Comment on the morphology of the erythrocytes.
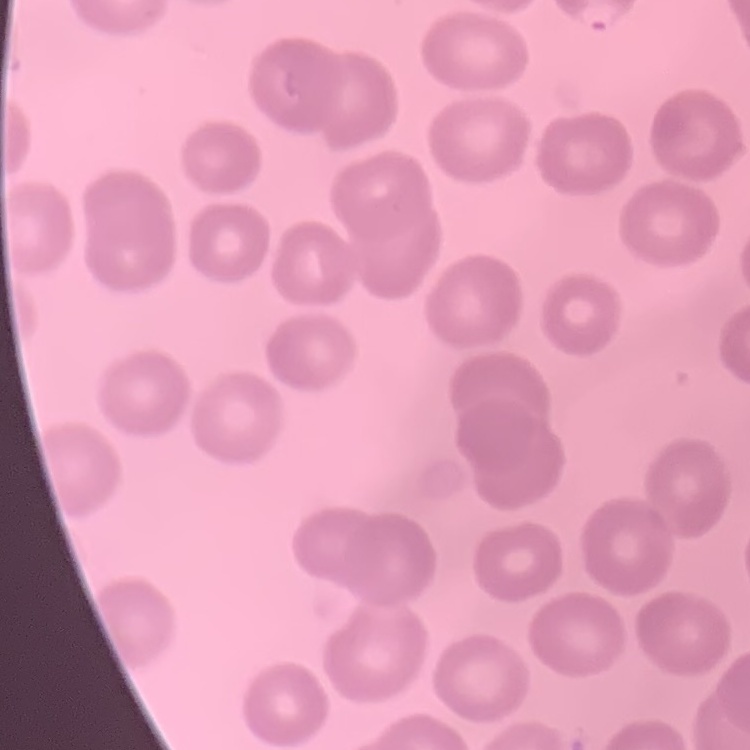
They show no rouleaux formation.

Summary:
  - Preparation: thin blood film
  - Image type: one tile cut from a larger photomicrograph
  - Stain: Field's or Giemsa